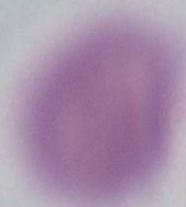
Summary:
  - Identification: erythrocyte
  - Magnification: 1000x
  - Modality: photomicrograph